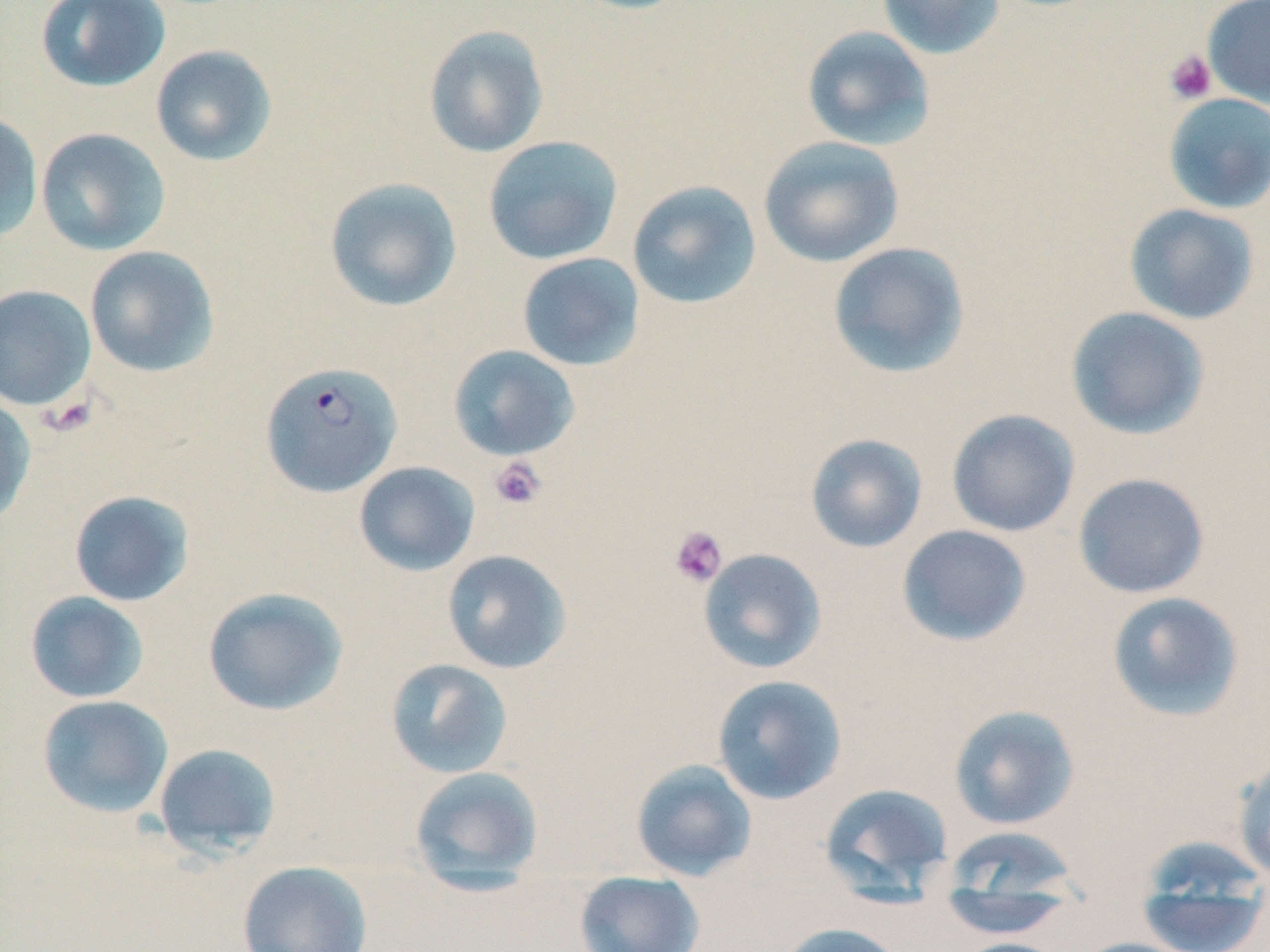

Summary:
  - Coordinate format: approximate bounding boxes as named x1/y1/x2/y2 corners in pixels
  - Plasmodium falciparum-infected red blood cell locations: (x1=260, y1=360, x2=403, y2=497)
  - Platelet locations: (x1=1164, y1=50, x2=1218, y2=105), (x1=39, y1=393, x2=99, y2=438), (x1=488, y1=456, x2=548, y2=510), (x1=668, y1=524, x2=729, y2=587)
  - Uninfected red blood cell locations: (x1=35, y1=0, x2=171, y2=92), (x1=569, y1=0, x2=696, y2=15), (x1=876, y1=0, x2=1007, y2=60), (x1=1202, y1=0, x2=1270, y2=108), (x1=423, y1=24, x2=549, y2=158), (x1=801, y1=25, x2=936, y2=152), (x1=150, y1=45, x2=278, y2=166), (x1=1162, y1=93, x2=1270, y2=214), (x1=0, y1=112, x2=43, y2=242), (x1=35, y1=128, x2=171, y2=256), (x1=482, y1=135, x2=623, y2=266), (x1=758, y1=136, x2=905, y2=268), (x1=324, y1=176, x2=462, y2=313), (x1=627, y1=180, x2=762, y2=309), (x1=1124, y1=203, x2=1261, y2=325), (x1=827, y1=242, x2=970, y2=379), (x1=84, y1=245, x2=220, y2=378), (x1=516, y1=252, x2=645, y2=371), (x1=0, y1=284, x2=96, y2=410), (x1=1065, y1=306, x2=1211, y2=440), (x1=448, y1=344, x2=581, y2=462), (x1=0, y1=395, x2=36, y2=527), (x1=946, y1=408, x2=1080, y2=537), (x1=805, y1=433, x2=928, y2=553), (x1=353, y1=461, x2=480, y2=576), (x1=1072, y1=472, x2=1211, y2=599), (x1=68, y1=490, x2=195, y2=607), (x1=896, y1=524, x2=1032, y2=647), (x1=698, y1=548, x2=827, y2=674), (x1=442, y1=549, x2=572, y2=674), (x1=202, y1=587, x2=350, y2=717), (x1=24, y1=591, x2=149, y2=704), (x1=1106, y1=591, x2=1246, y2=722), (x1=384, y1=658, x2=515, y2=779), (x1=711, y1=674, x2=847, y2=805), (x1=36, y1=694, x2=174, y2=818), (x1=948, y1=704, x2=1081, y2=830), (x1=153, y1=742, x2=282, y2=858), (x1=1232, y1=752, x2=1270, y2=885), (x1=631, y1=758, x2=757, y2=881), (x1=408, y1=766, x2=545, y2=892), (x1=820, y1=783, x2=955, y2=898), (x1=941, y1=825, x2=1084, y2=909), (x1=1134, y1=840, x2=1270, y2=952), (x1=237, y1=860, x2=373, y2=952), (x1=574, y1=870, x2=705, y2=952), (x1=936, y1=887, x2=1075, y2=939), (x1=776, y1=922, x2=907, y2=952), (x1=1070, y1=937, x2=1200, y2=952), (x1=947, y1=938, x2=1073, y2=952)
  - Slide-level diagnosis: Plasmodium falciparum
  - Image size: 1270×952 pixels
  - Modality: light microscopy
  - Field of view: single
  - Preparation: thin blood film
  - Stain: May-Grünwald-Giemsa
  - Magnification: 1000x